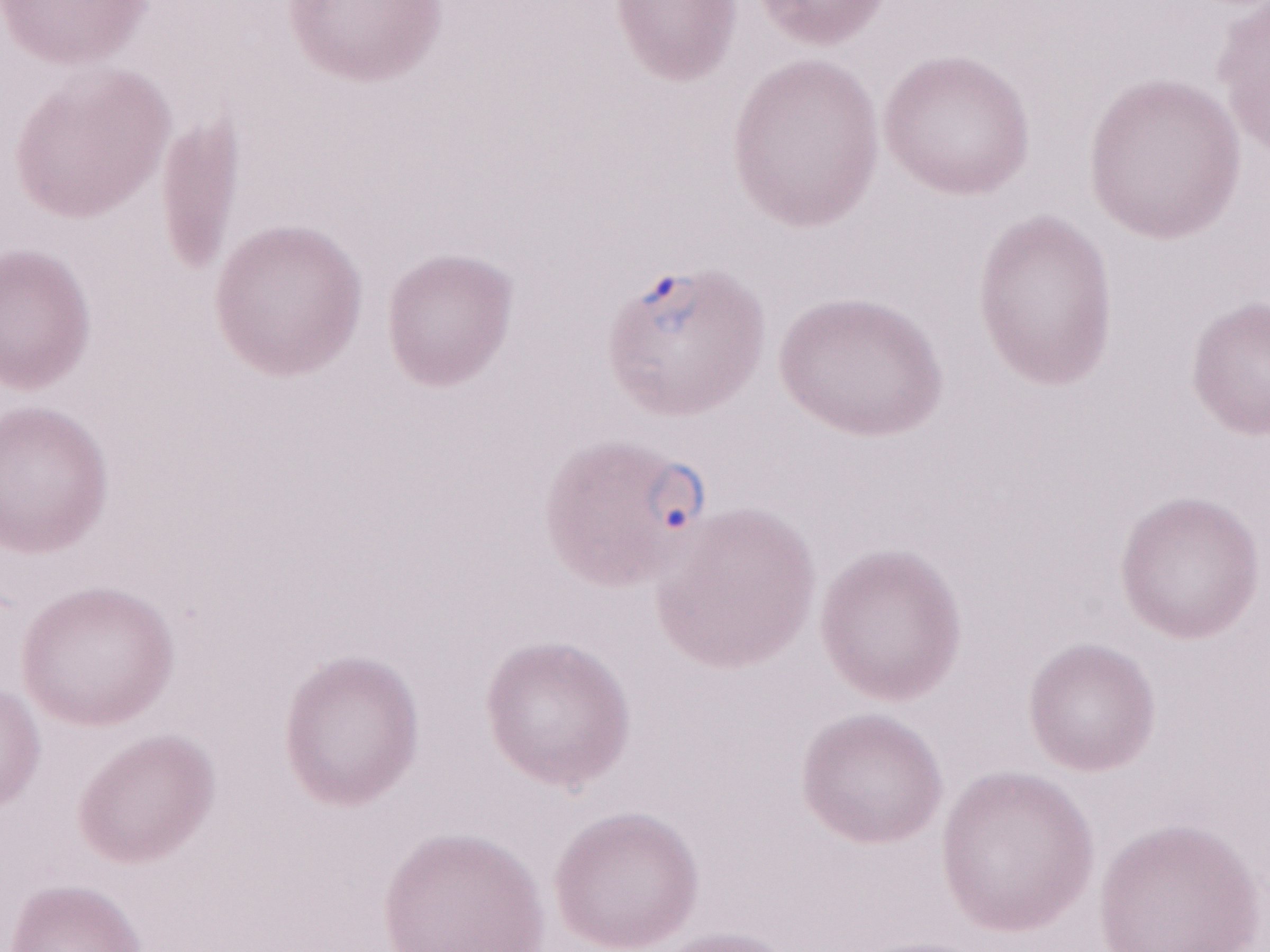
Image is 1270×952 pixels. 1,000x magnification. May-Grünwald-Giemsa stain. Thin blood film. Olympus BX43 microscope, Olympus DP73 camera. Patient diagnosis: malaria infection. Single field of view.